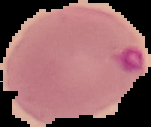

Summary:
  - Result: Plasmodium parasites identified
  - Preparation: thin blood film
  - Image type: segmented cell region on a black background
  - Image size: 151×127 pixels